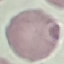

Malaria status: uninfected. Giemsa-stained preparation. Photographed with a smartphone camera at the microscope eyepiece. Thin blood film. Automatically extracted cell patch, resized to 64 × 64 pixels.